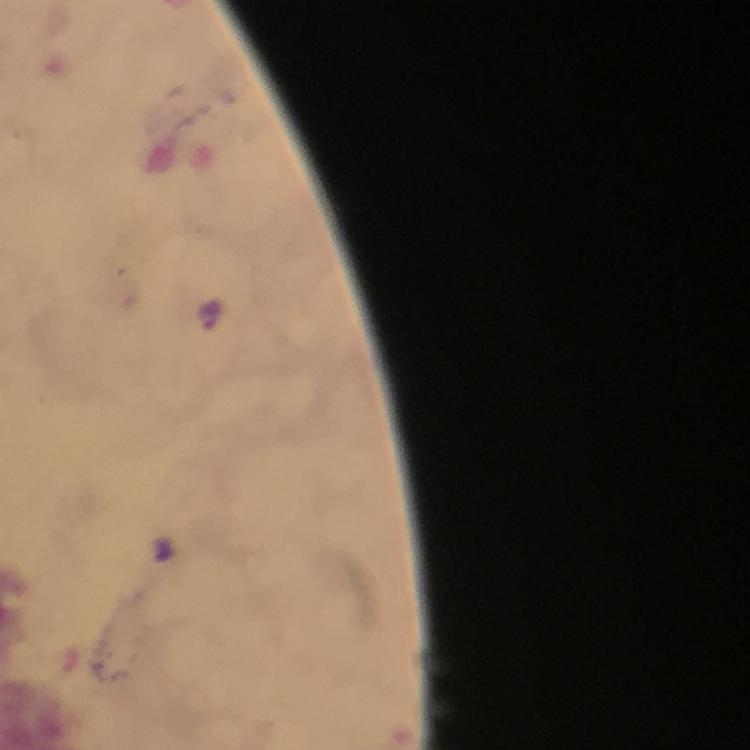

Approximate centers as (x, y) in pixels. Malaria parasite locations: (213, 315). Cropped region of a single field of view. Thick smear. 100x magnification. Immersion oil applied. From a malaria diagnostic workup. Giemsa-stained preparation. Photographed with a smartphone mounted on the microscope. Image is 750×750 pixels.